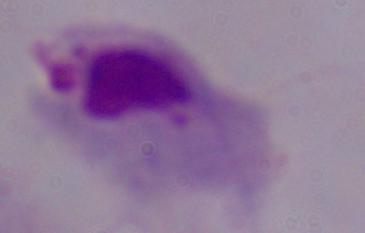
Micrograph. Captured at 1000x magnification. A trichomonad is shown.